State which parasite is depicted.
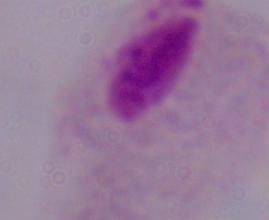

A trichomonad.

magnification = 1000x
modality = photomicrograph